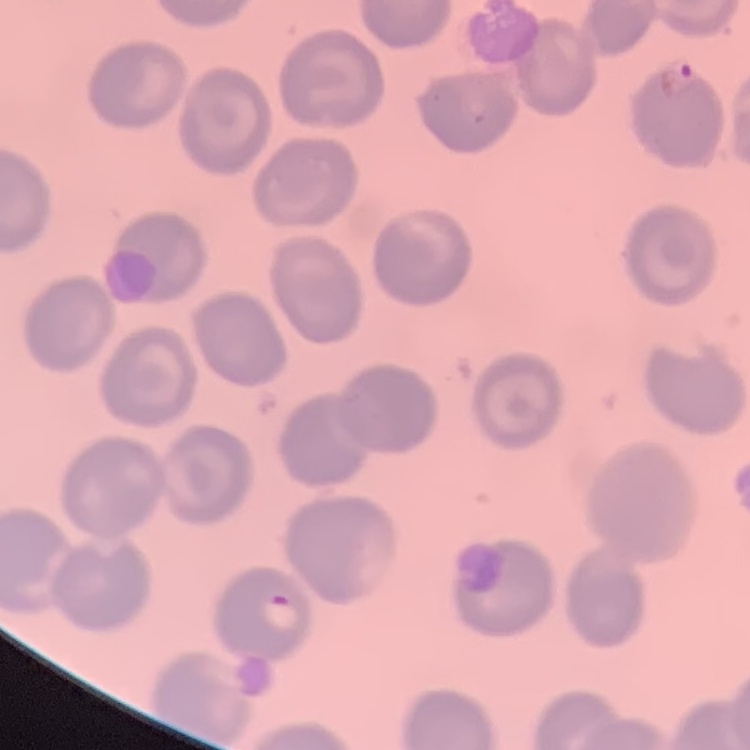 The erythrocytes exhibit no rouleaux formation. Square crop of a larger photomicrograph. Thin blood film. Stained with either Field's or Giemsa.